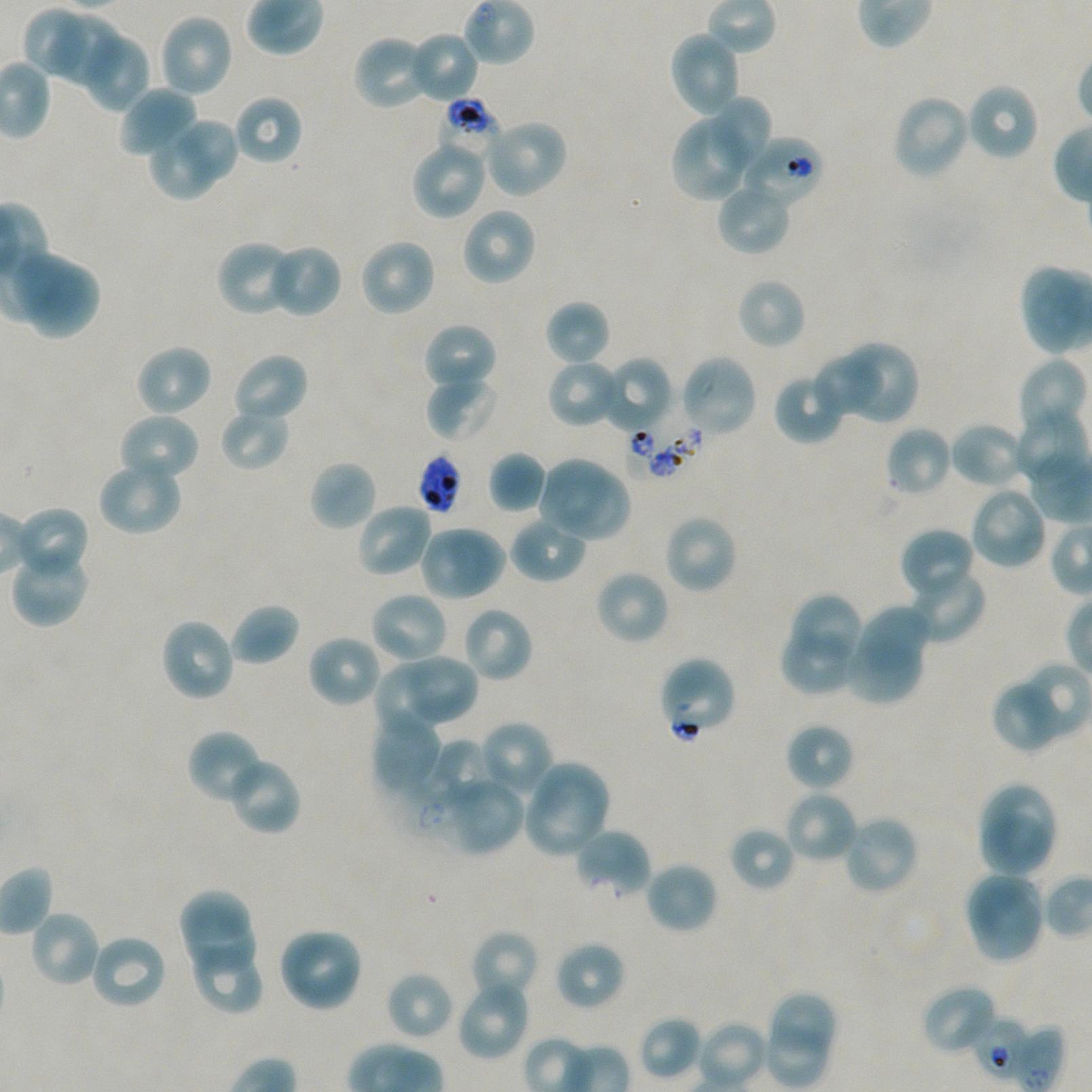
Not every red blood cell is marked. A life-cycle stage — or a range of stages, where the recorded stages span more than one — follows each staged infected red blood cell.
locations of red blood cells of indeterminate infection status = approximate bounding rectangles given as corner coordinates in pixels from the top-left: (x1=437, y1=98, x2=505, y2=164), (x1=740, y1=134, x2=824, y2=210), (x1=625, y1=417, x2=704, y2=480), (x1=656, y1=655, x2=738, y2=740), (x1=1011, y1=1025, x2=1066, y2=1092)
field of view = one from this slide
image size = 1092×1092 pixels
locations of uninfected red blood cells = approximate bounding rectangles given as corner coordinates in pixels from the top-left: (x1=24, y1=6, x2=84, y2=75), (x1=158, y1=13, x2=234, y2=98), (x1=52, y1=16, x2=118, y2=84), (x1=668, y1=29, x2=742, y2=119), (x1=407, y1=31, x2=480, y2=103), (x1=352, y1=33, x2=433, y2=111), (x1=84, y1=35, x2=151, y2=113), (x1=966, y1=82, x2=1040, y2=162), (x1=117, y1=85, x2=198, y2=160), (x1=892, y1=93, x2=971, y2=180), (x1=234, y1=94, x2=303, y2=166), (x1=714, y1=96, x2=774, y2=161), (x1=670, y1=110, x2=757, y2=202), (x1=482, y1=117, x2=568, y2=199), (x1=179, y1=120, x2=238, y2=179), (x1=151, y1=138, x2=215, y2=200), (x1=410, y1=139, x2=489, y2=220), (x1=715, y1=181, x2=792, y2=255), (x1=459, y1=206, x2=536, y2=287), (x1=359, y1=237, x2=437, y2=318), (x1=216, y1=240, x2=291, y2=314), (x1=274, y1=247, x2=341, y2=315), (x1=8, y1=249, x2=102, y2=340), (x1=1022, y1=266, x2=1084, y2=357), (x1=736, y1=277, x2=807, y2=350), (x1=545, y1=300, x2=611, y2=367), (x1=422, y1=321, x2=498, y2=393), (x1=843, y1=341, x2=918, y2=421), (x1=134, y1=344, x2=213, y2=418), (x1=231, y1=352, x2=310, y2=424), (x1=678, y1=354, x2=759, y2=439), (x1=598, y1=357, x2=674, y2=435), (x1=547, y1=358, x2=623, y2=429), (x1=814, y1=358, x2=886, y2=418), (x1=1017, y1=359, x2=1085, y2=426), (x1=425, y1=373, x2=499, y2=442), (x1=773, y1=380, x2=839, y2=445), (x1=219, y1=407, x2=291, y2=471), (x1=1011, y1=408, x2=1088, y2=488), (x1=117, y1=412, x2=200, y2=486), (x1=949, y1=420, x2=1029, y2=490), (x1=885, y1=425, x2=953, y2=498), (x1=488, y1=451, x2=547, y2=513), (x1=1029, y1=455, x2=1091, y2=522), (x1=96, y1=457, x2=183, y2=537), (x1=308, y1=460, x2=378, y2=532), (x1=536, y1=462, x2=604, y2=527), (x1=560, y1=473, x2=632, y2=543), (x1=967, y1=486, x2=1048, y2=570), (x1=354, y1=502, x2=434, y2=579), (x1=18, y1=507, x2=90, y2=570), (x1=663, y1=513, x2=738, y2=594), (x1=508, y1=515, x2=588, y2=584), (x1=418, y1=524, x2=507, y2=602), (x1=899, y1=526, x2=976, y2=602), (x1=12, y1=556, x2=90, y2=625), (x1=906, y1=566, x2=986, y2=645), (x1=594, y1=568, x2=670, y2=645), (x1=369, y1=590, x2=449, y2=666), (x1=793, y1=594, x2=861, y2=660), (x1=228, y1=602, x2=300, y2=667), (x1=461, y1=606, x2=534, y2=683), (x1=858, y1=606, x2=928, y2=666), (x1=159, y1=617, x2=236, y2=703), (x1=306, y1=633, x2=384, y2=709), (x1=780, y1=634, x2=854, y2=695), (x1=843, y1=641, x2=923, y2=704), (x1=407, y1=653, x2=478, y2=723), (x1=1013, y1=662, x2=1092, y2=743), (x1=374, y1=666, x2=447, y2=733), (x1=991, y1=678, x2=1062, y2=753), (x1=374, y1=715, x2=439, y2=789), (x1=478, y1=720, x2=554, y2=799), (x1=784, y1=722, x2=855, y2=792), (x1=186, y1=729, x2=266, y2=805), (x1=435, y1=740, x2=491, y2=802), (x1=226, y1=756, x2=302, y2=837), (x1=537, y1=763, x2=611, y2=827), (x1=438, y1=773, x2=525, y2=856), (x1=522, y1=774, x2=606, y2=858), (x1=981, y1=785, x2=1059, y2=854), (x1=784, y1=790, x2=859, y2=864), (x1=982, y1=812, x2=1051, y2=876), (x1=840, y1=814, x2=920, y2=897), (x1=729, y1=826, x2=795, y2=892), (x1=573, y1=828, x2=652, y2=899), (x1=644, y1=861, x2=718, y2=935), (x1=968, y1=880, x2=1037, y2=959), (x1=177, y1=888, x2=249, y2=938), (x1=28, y1=909, x2=102, y2=988), (x1=187, y1=913, x2=256, y2=968), (x1=278, y1=926, x2=365, y2=1013), (x1=470, y1=930, x2=540, y2=1004), (x1=88, y1=933, x2=168, y2=1010), (x1=555, y1=940, x2=626, y2=1011), (x1=196, y1=956, x2=263, y2=1016), (x1=384, y1=971, x2=454, y2=1041), (x1=456, y1=977, x2=532, y2=1062), (x1=921, y1=983, x2=1000, y2=1057), (x1=774, y1=991, x2=838, y2=1052), (x1=640, y1=1016, x2=702, y2=1079), (x1=697, y1=1020, x2=769, y2=1090), (x1=769, y1=1026, x2=825, y2=1084)
objective = 100x, oil immersion, numerical aperture 1.45
culture = static in-vitro P. falciparum strain NF54
donor blood group = A+/O+
locations of infected red blood cells = approximate bounding rectangles given as corner coordinates in pixels from the top-left: (x1=973, y1=1017, x2=1038, y2=1083) early ring to early trophozoite
stain = Giemsa
preparation = thin blood film